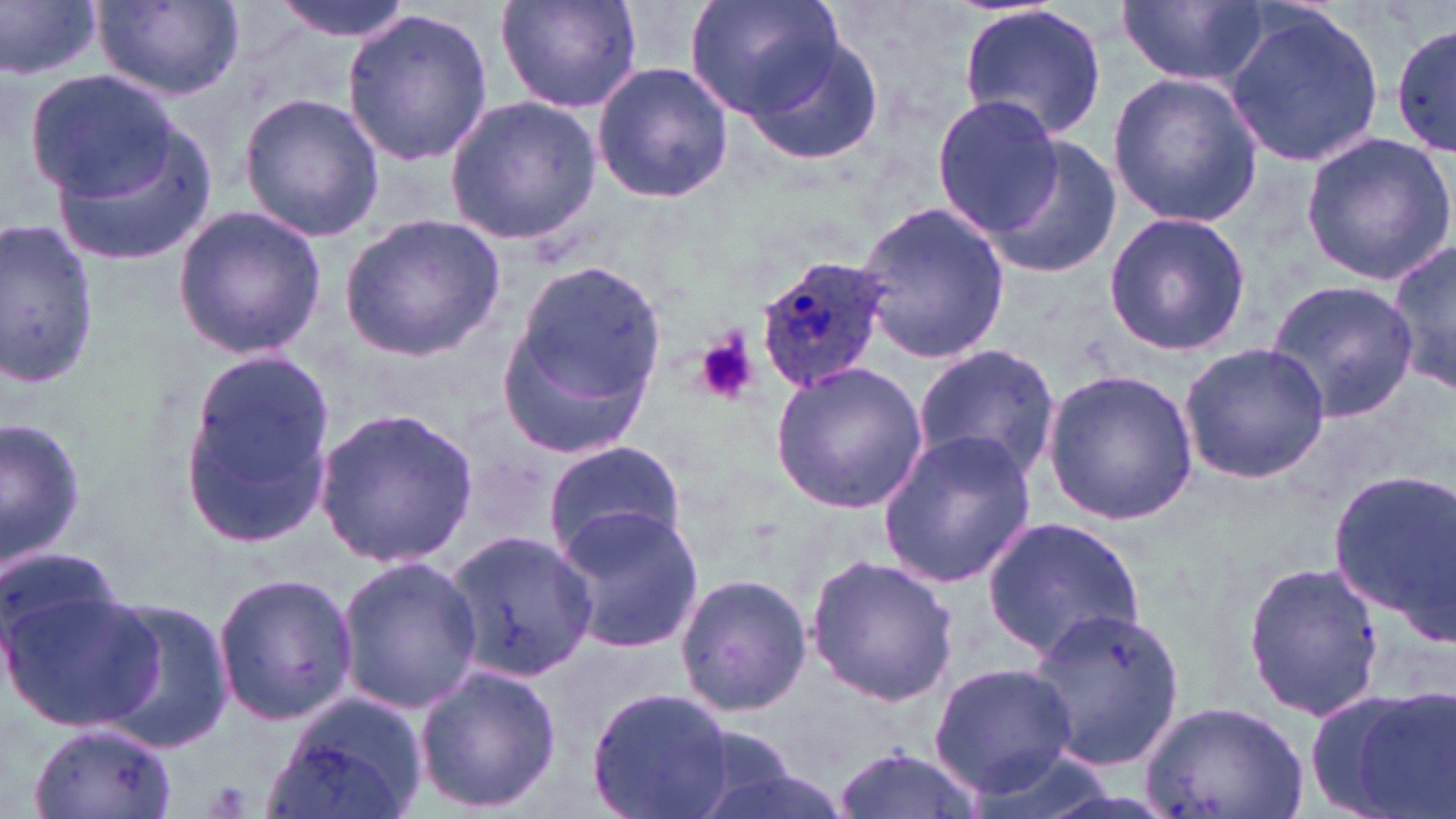
Summary:
  - Coordinate format: approximate bounding boxes as (x1, y1, x2, y2) in pixels
  - Uninfected red blood cell locations: (1, 0, 103, 82), (269, 0, 415, 41), (495, 0, 648, 113), (685, 0, 845, 120), (1117, 1, 1270, 88), (94, 2, 241, 100), (957, 4, 1108, 143), (340, 8, 492, 167), (1224, 9, 1387, 168), (1391, 24, 1456, 160), (740, 30, 886, 169), (592, 62, 734, 202), (24, 66, 187, 214), (1107, 72, 1264, 228), (237, 91, 385, 242), (444, 95, 600, 246), (931, 96, 1062, 237), (47, 111, 220, 272), (1299, 132, 1456, 285), (983, 134, 1122, 279), (856, 202, 1011, 363), (170, 204, 328, 359), (1103, 211, 1249, 357), (339, 215, 506, 360), (0, 216, 101, 392), (1386, 232, 1454, 400), (500, 256, 669, 455), (1266, 276, 1418, 422), (1177, 341, 1330, 485), (914, 344, 1064, 482), (176, 347, 340, 548), (770, 362, 929, 514), (1042, 369, 1199, 527), (313, 404, 479, 571), (2, 414, 89, 576), (876, 431, 1037, 588), (543, 439, 687, 560), (1325, 467, 1454, 632), (548, 505, 704, 653), (983, 515, 1147, 659), (444, 531, 598, 685), (0, 542, 135, 674), (806, 554, 958, 707), (335, 557, 483, 714), (1243, 559, 1386, 720), (211, 567, 358, 727), (675, 571, 811, 719), (0, 574, 158, 734), (90, 596, 234, 754), (1023, 604, 1187, 770), (928, 660, 1079, 801), (413, 663, 561, 815), (1302, 682, 1452, 819), (586, 687, 736, 819), (264, 691, 428, 819), (1136, 697, 1312, 819), (29, 726, 174, 817), (677, 729, 837, 819), (831, 749, 985, 819)
  - Plasmodium ovale-infected red blood cell locations: (756, 249, 894, 393)
  - Platelet locations: (695, 327, 757, 406)
  - Slide-level diagnosis: Plasmodium ovale
  - Preparation: thin blood film
  - Stain: May-Grünwald-Giemsa
  - Modality: optical microscopy
  - Magnification: 1000x
  - Image size: 1456×819 pixels
  - Field of view: one of a larger specimen